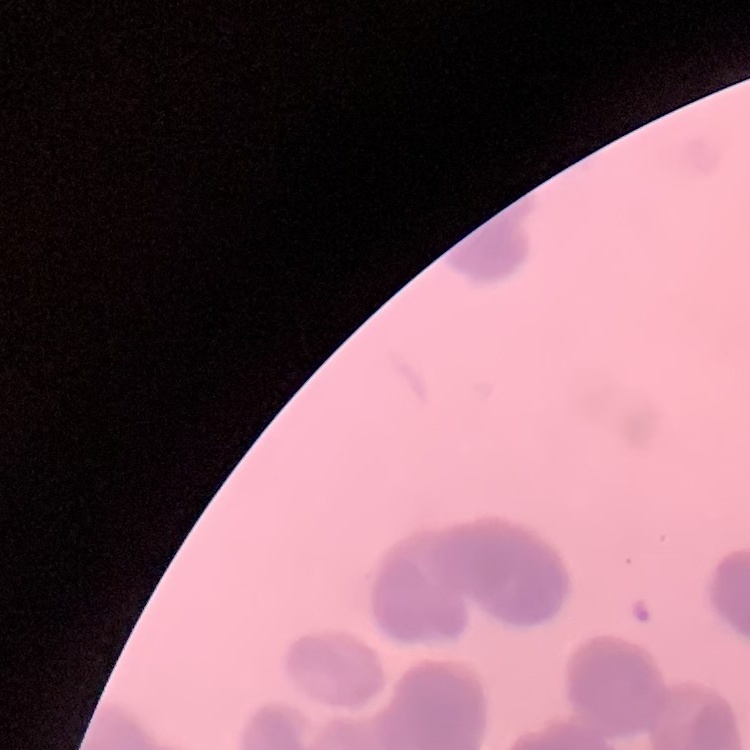

Summary:
  - Red blood cell morphology: rouleaux formation
  - Stain: Field's or Giemsa
  - Preparation: thin blood film
  - Image type: one tile cut from a larger photomicrograph